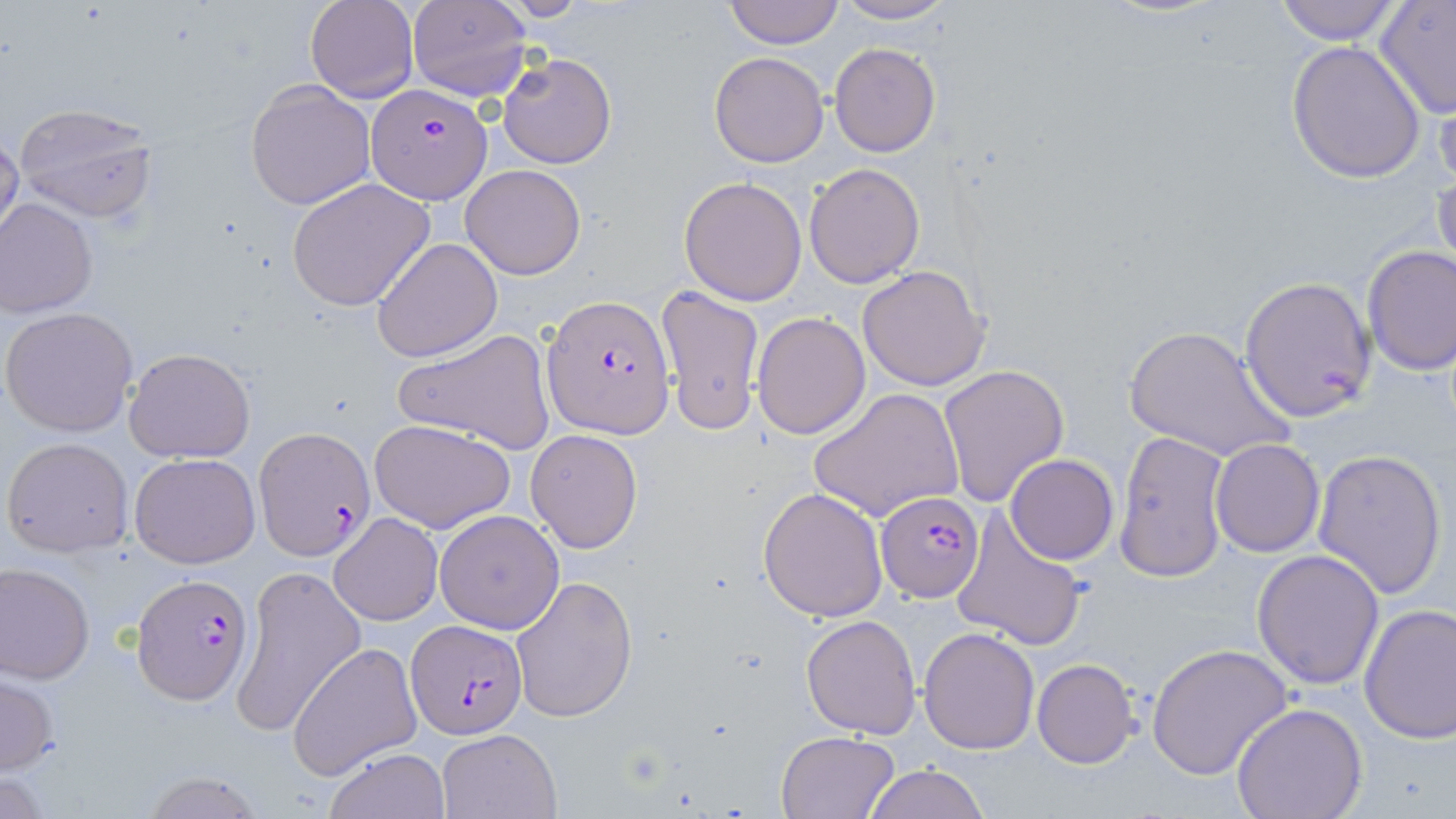
Approximate bounding boxes as (x1, y1, x2, y2) in pixels. Plasmodium falciparum-infected red blood cell locations: (366, 81, 493, 203), (542, 295, 675, 437), (256, 427, 375, 560), (876, 492, 983, 602), (131, 573, 253, 703), (404, 619, 526, 739). Uninfected red blood cell locations: (305, 0, 418, 102), (407, 0, 532, 102), (722, 0, 843, 48), (833, 1, 956, 24), (1269, 1, 1405, 45), (1374, 1, 1456, 119), (1284, 39, 1426, 183), (829, 42, 940, 157), (497, 52, 616, 169), (709, 52, 828, 168), (1431, 78, 1456, 194), (245, 79, 377, 210), (12, 102, 158, 224), (0, 129, 23, 246), (804, 163, 925, 288), (462, 165, 584, 279), (1433, 169, 1456, 282), (679, 175, 807, 305), (287, 178, 435, 311), (1, 198, 98, 317), (370, 236, 502, 361), (1361, 245, 1456, 375), (859, 265, 990, 391), (1239, 275, 1378, 422), (656, 284, 764, 435), (1, 306, 138, 436), (751, 311, 871, 440), (1122, 325, 1295, 463), (393, 327, 559, 456), (124, 347, 256, 462), (938, 364, 1071, 507), (809, 388, 964, 522), (370, 418, 517, 534), (525, 428, 643, 554), (1113, 429, 1232, 583), (3, 436, 134, 558), (1210, 438, 1325, 556), (1311, 448, 1447, 601), (130, 454, 258, 569), (1005, 455, 1120, 565), (757, 486, 888, 622), (950, 507, 1087, 652), (433, 511, 564, 635), (329, 512, 443, 626), (1251, 549, 1386, 689), (0, 562, 95, 683), (230, 565, 366, 737), (510, 576, 638, 721), (1357, 600, 1456, 745), (800, 614, 922, 737), (918, 626, 1040, 755), (1148, 641, 1293, 780), (288, 642, 423, 778), (1032, 658, 1141, 768), (1, 671, 59, 776), (1230, 702, 1369, 819), (436, 729, 561, 818), (775, 732, 899, 817), (324, 747, 450, 819), (862, 763, 989, 819), (137, 771, 268, 818). Slide-level diagnosis: Plasmodium falciparum. May-Grünwald-Giemsa stain. Image is 1456×819 pixels. One field of a larger specimen. Optical microscopy. Thin blood smear. Captured at 1000x magnification.